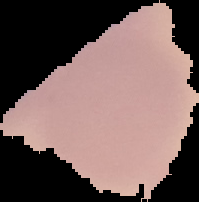

preparation = thin blood film
malaria status = uninfected
image size = 199×202 pixels
image type = cell region segmented out of the field of view; surrounding area masked to black